State the blood parasite species.
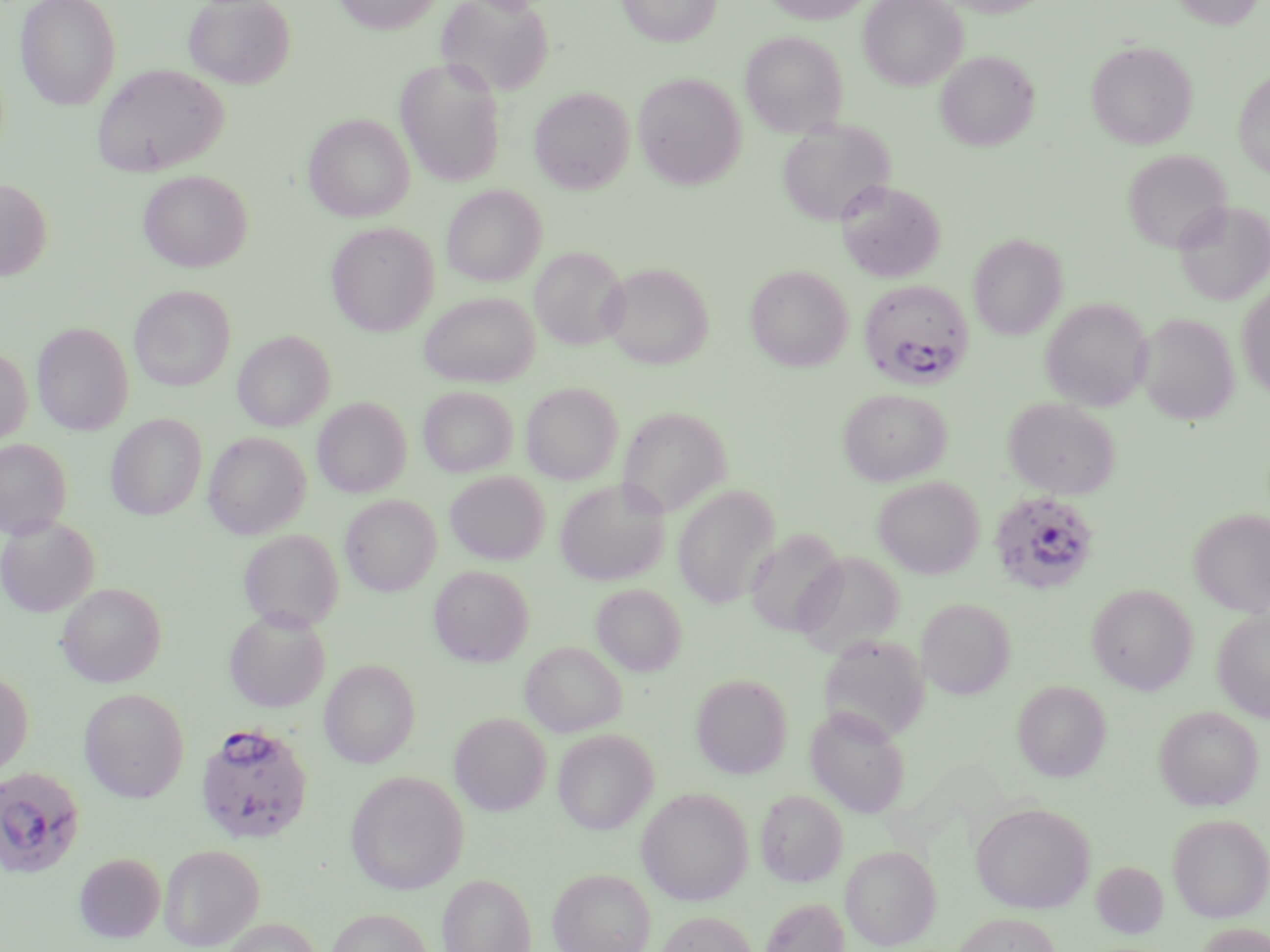

Plasmodium falciparum.

{
  "preparation": "thin blood smear",
  "uninfected_red_blood_cell_locations": "approximate bounding boxes as (x1, y1, x2, y2) in pixels: (15, 0, 122, 110), (183, 0, 295, 89), (333, 0, 444, 34), (436, 0, 554, 99), (617, 0, 721, 47), (763, 0, 875, 24), (859, 0, 966, 90), (1167, 0, 1264, 29), (740, 31, 847, 138), (1086, 41, 1197, 149), (935, 51, 1039, 151), (396, 58, 506, 187), (92, 63, 227, 177), (1233, 68, 1270, 179), (633, 72, 747, 189), (529, 87, 635, 193), (304, 114, 414, 222), (776, 119, 894, 228), (1122, 148, 1232, 254), (138, 170, 252, 272), (0, 178, 53, 281), (836, 180, 946, 283), (441, 184, 546, 286), (1173, 200, 1270, 306), (326, 222, 439, 337), (968, 233, 1067, 340), (531, 246, 628, 351), (602, 262, 713, 369), (746, 264, 853, 371), (1237, 284, 1270, 399), (129, 285, 235, 391), (419, 291, 539, 387), (1040, 297, 1152, 411), (1136, 312, 1239, 425), (33, 322, 133, 435), (233, 330, 334, 431), (0, 346, 32, 445), (521, 382, 622, 484), (418, 386, 517, 477), (838, 388, 951, 485), (1003, 397, 1120, 499), (313, 398, 411, 498), (618, 406, 733, 518), (106, 414, 207, 520), (204, 432, 311, 538), (0, 438, 72, 539), (445, 471, 550, 565), (873, 476, 984, 578), (554, 479, 671, 586), (673, 484, 780, 609), (340, 495, 441, 596), (1189, 508, 1270, 617), (0, 515, 100, 617), (238, 529, 343, 632), (745, 529, 846, 637), (794, 551, 904, 657), (429, 565, 534, 666), (57, 582, 167, 688), (591, 583, 687, 676), (1086, 583, 1197, 695), (917, 598, 1015, 700), (224, 607, 331, 712), (1212, 608, 1270, 721), (818, 633, 931, 743), (520, 641, 627, 736), (320, 659, 421, 767), (0, 671, 33, 778), (691, 673, 793, 778), (1012, 680, 1111, 782), (79, 688, 190, 802), (1154, 705, 1263, 811), (805, 706, 910, 817), (450, 712, 551, 816), (552, 728, 659, 834), (345, 770, 469, 894), (636, 787, 754, 905), (755, 788, 848, 887), (970, 801, 1095, 913), (1167, 813, 1270, 922), (158, 844, 265, 950), (841, 844, 942, 949), (74, 852, 166, 943), (1092, 861, 1168, 938), (548, 867, 655, 952), (438, 873, 537, 952), (758, 896, 850, 952), (325, 908, 435, 952), (656, 910, 759, 952), (953, 912, 1061, 951), (215, 917, 323, 952), (1195, 922, 1270, 952)",
  "stain": "May-Grünwald-Giemsa",
  "modality": "optical microscopy",
  "image_size": "1270×952 pixels",
  "magnification": "1000x",
  "field_of_view": "single",
  "plasmodium_falciparum_infected_red_blood_cell_locations": "approximate bounding boxes as (x1, y1, x2, y2) in pixels: (858, 279, 974, 389), (989, 490, 1101, 596), (194, 722, 314, 845), (0, 766, 87, 880)"
}